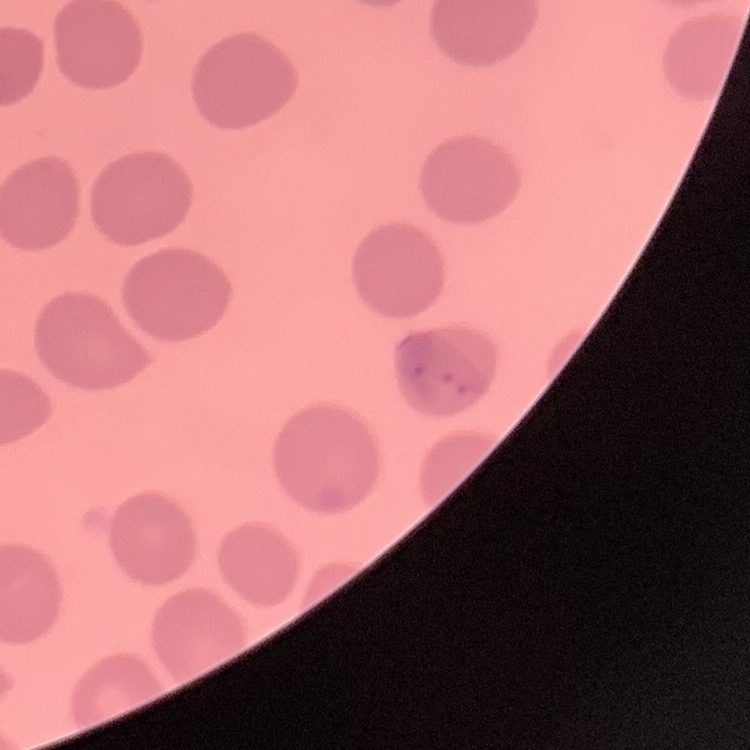

erythrocyte morphology = no rouleaux formation
preparation = thin peripheral smear
image type = square crop of a larger photomicrograph
stain = Field's or Giemsa